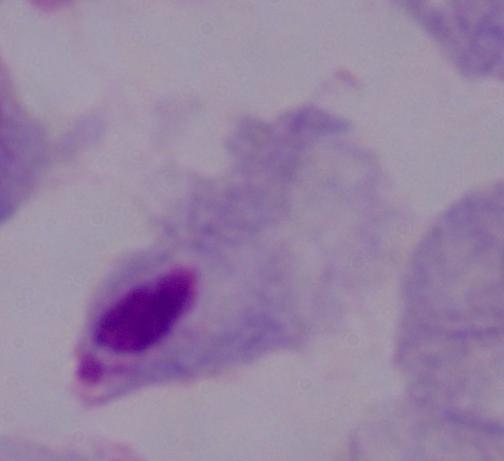

identification = trichomonad
modality = photomicrograph
magnification = 1000x